Give the extent of all Plasmodium malariae-infected red blood cells.
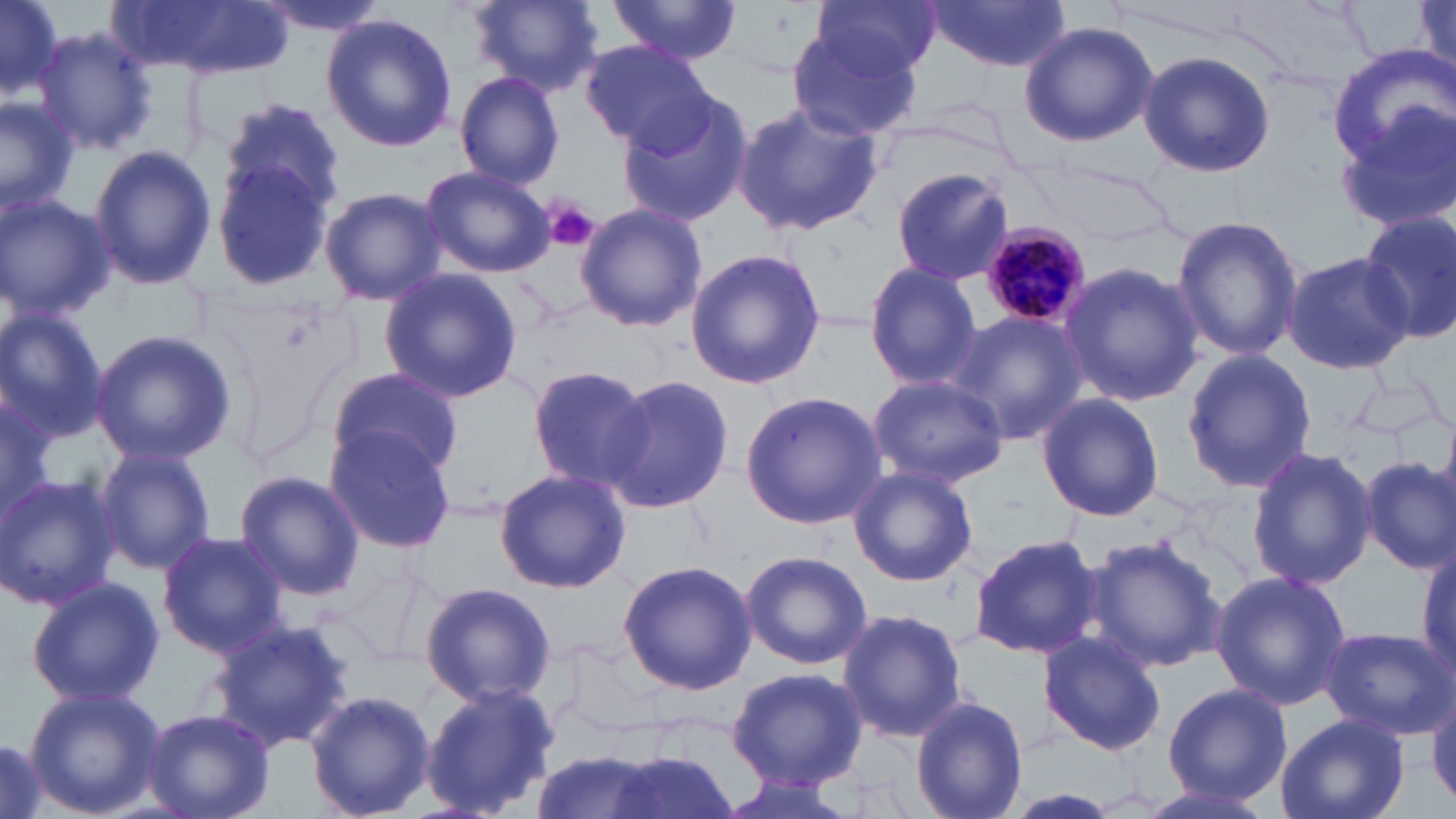
Approximate bounding boxes as [x1, y1, x2, y2] in pixels.
Plasmodium malariae-infected red blood cells: [979, 222, 1090, 329].

slide-level diagnosis = Plasmodium malariae
uninfected red blood cell locations = approximate bounding boxes as [x1, y1, x2, y2] in pixels: [0, 0, 67, 109], [251, 0, 390, 36], [468, 0, 603, 96], [609, 0, 742, 64], [815, 0, 941, 77], [928, 1, 1070, 72], [132, 2, 294, 77], [1414, 2, 1455, 75], [322, 13, 456, 154], [1017, 20, 1156, 147], [32, 28, 158, 156], [789, 28, 919, 141], [582, 39, 713, 152], [1327, 48, 1456, 178], [1137, 49, 1275, 178], [454, 70, 565, 188], [1334, 91, 1456, 238], [0, 93, 80, 219], [617, 94, 752, 229], [222, 99, 347, 214], [731, 100, 884, 237], [88, 144, 216, 290], [209, 156, 338, 293], [419, 163, 555, 277], [889, 167, 1016, 287], [320, 187, 446, 307], [0, 193, 114, 321], [575, 203, 706, 333], [1358, 212, 1456, 346], [1170, 214, 1304, 363], [684, 247, 827, 391], [1282, 251, 1414, 375], [1057, 260, 1204, 407], [864, 262, 983, 390], [378, 269, 522, 403], [0, 308, 111, 444], [947, 309, 1089, 448], [88, 329, 237, 467], [1181, 349, 1317, 493], [526, 365, 656, 494], [326, 367, 466, 482], [866, 374, 1009, 488], [604, 375, 732, 514], [740, 390, 886, 529], [1036, 392, 1164, 521], [0, 395, 59, 524], [325, 426, 456, 555], [93, 444, 217, 575], [1244, 448, 1375, 589], [1357, 455, 1456, 574], [848, 465, 978, 587], [494, 468, 630, 595], [233, 470, 365, 600], [0, 474, 121, 612], [156, 531, 290, 657], [969, 532, 1104, 660], [1081, 534, 1226, 673], [1413, 540, 1456, 683], [740, 550, 872, 670], [619, 559, 757, 694], [1210, 569, 1352, 710], [26, 576, 164, 708], [420, 581, 555, 707], [837, 607, 967, 742], [210, 619, 356, 753], [1319, 625, 1453, 738], [1037, 630, 1168, 754], [726, 666, 866, 790], [1426, 679, 1456, 811], [419, 682, 559, 819], [1163, 683, 1291, 802], [24, 685, 165, 818], [304, 689, 436, 819], [910, 694, 1030, 819], [142, 708, 275, 819], [1274, 712, 1410, 819], [0, 732, 51, 819], [528, 749, 667, 819], [593, 749, 742, 819], [716, 772, 862, 819], [1131, 779, 1281, 819]
platelet locations = approximate bounding boxes as [x1, y1, x2, y2] in pixels: [544, 202, 599, 252]
modality = optical microscopy
magnification = 1000x
field of view = one of a larger specimen
preparation = thin blood smear
image size = 1456×819 pixels
stain = May-Grünwald-Giemsa